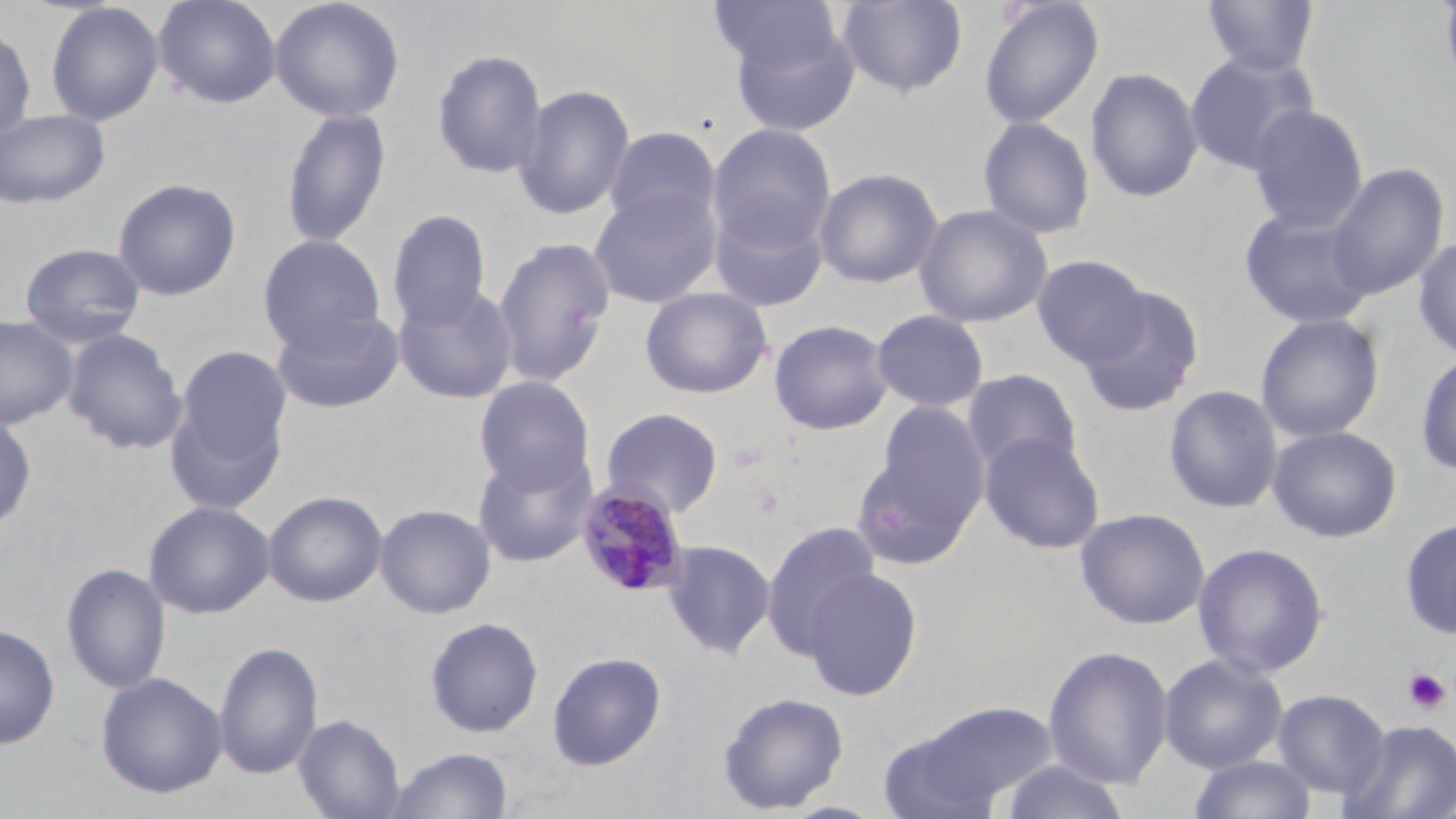
Summary:
  - Coordinate format: approximate bounding boxes as [x1, y1, x2, y2] in pixels
  - Plasmodium malariae-infected red blood cell locations: [575, 481, 689, 598]
  - Uninfected red blood cell locations: [153, 0, 282, 109], [270, 0, 405, 123], [708, 0, 842, 77], [836, 0, 968, 98], [978, 0, 1104, 129], [1200, 0, 1320, 77], [1437, 0, 1456, 99], [44, 2, 165, 127], [0, 22, 37, 142], [731, 22, 861, 138], [431, 48, 548, 179], [1184, 51, 1316, 175], [1085, 66, 1203, 203], [514, 84, 635, 220], [1247, 103, 1369, 233], [281, 107, 392, 249], [0, 109, 110, 209], [977, 116, 1095, 239], [707, 124, 837, 260], [603, 126, 721, 234], [1325, 163, 1448, 301], [814, 168, 942, 288], [112, 177, 241, 301], [588, 186, 721, 308], [711, 198, 832, 313], [914, 203, 1053, 327], [1238, 207, 1376, 328], [387, 210, 492, 331], [258, 235, 386, 355], [491, 235, 616, 387], [1413, 235, 1456, 361], [19, 242, 147, 347], [1032, 255, 1150, 366], [394, 283, 519, 405], [1076, 285, 1205, 418], [640, 287, 773, 399], [270, 307, 405, 414], [871, 309, 989, 413], [1254, 312, 1385, 443], [0, 315, 77, 429], [769, 318, 894, 435], [62, 328, 187, 454], [170, 346, 291, 503], [1415, 351, 1456, 477], [962, 369, 1082, 474], [474, 376, 596, 494], [1163, 384, 1283, 514], [860, 400, 990, 561], [600, 407, 724, 518], [0, 411, 36, 534], [1267, 425, 1402, 542], [979, 432, 1105, 554], [473, 445, 597, 567], [263, 490, 387, 607], [144, 500, 275, 619], [375, 503, 496, 618], [1075, 507, 1211, 629], [1399, 516, 1456, 639], [761, 521, 882, 658], [661, 539, 775, 659], [1192, 541, 1330, 679], [61, 563, 171, 695], [802, 566, 924, 701], [424, 617, 544, 738], [0, 623, 60, 750], [213, 640, 323, 781], [1043, 644, 1174, 790], [547, 651, 666, 771], [1158, 653, 1288, 773], [95, 672, 227, 799], [1272, 689, 1390, 800], [717, 690, 849, 814], [911, 700, 1059, 808], [294, 713, 405, 819], [1341, 719, 1456, 819], [877, 726, 1001, 819], [386, 747, 514, 819], [1187, 754, 1317, 818], [998, 759, 1131, 819]
  - Platelet locations: [874, 505, 907, 540], [1403, 667, 1452, 715]
  - Slide-level diagnosis: Plasmodium malariae
  - Preparation: thin blood smear
  - Modality: light microscopy
  - Magnification: 1000x
  - Field of view: single
  - Stain: May-Grünwald-Giemsa
  - Image size: 1456×819 pixels